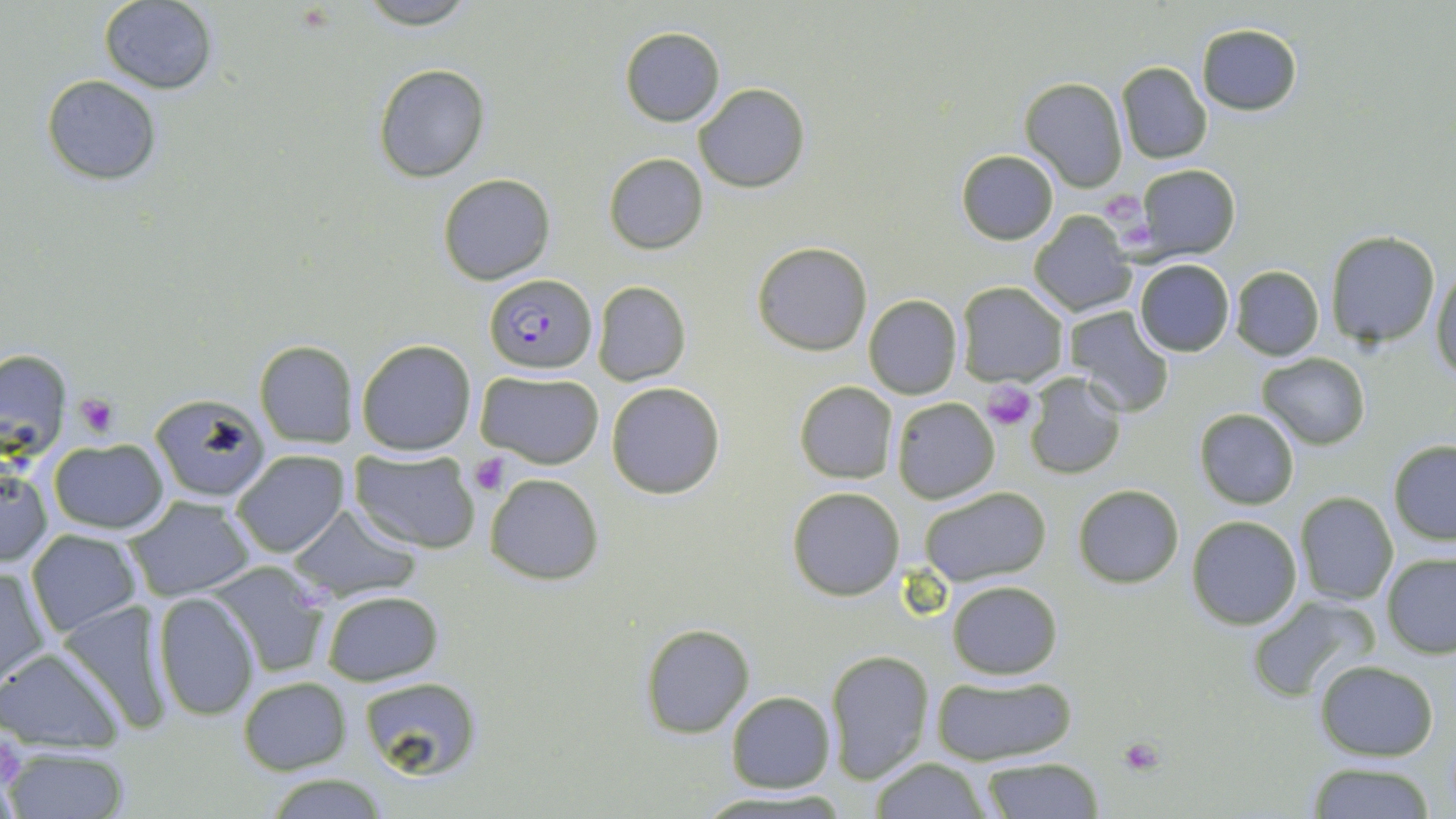
Approximate bounding boxes as [x1, y1, x2, y2] in pixels. Plasmodium falciparum-infected red blood cell locations: [484, 273, 595, 373]. Uninfected red blood cell locations: [353, 0, 482, 28], [98, 1, 219, 93], [1197, 22, 1303, 116], [619, 27, 726, 127], [1116, 61, 1210, 165], [374, 64, 490, 182], [41, 74, 161, 185], [1019, 76, 1128, 191], [694, 83, 810, 193], [955, 149, 1058, 244], [604, 153, 709, 254], [1135, 162, 1239, 259], [438, 173, 555, 284], [1028, 210, 1136, 317], [1325, 231, 1439, 347], [752, 241, 873, 355], [1133, 259, 1234, 357], [1430, 265, 1456, 382], [1230, 266, 1324, 359], [591, 281, 691, 386], [956, 281, 1068, 387], [863, 295, 962, 400], [1061, 306, 1174, 418], [255, 339, 357, 447], [356, 339, 475, 455], [0, 349, 72, 462], [1257, 353, 1369, 450], [474, 369, 606, 468], [1025, 374, 1125, 480], [795, 381, 897, 484], [605, 382, 725, 498], [147, 390, 273, 504], [891, 396, 1001, 504], [1194, 409, 1300, 510], [46, 439, 170, 534], [1388, 439, 1456, 545], [230, 448, 350, 559], [350, 449, 480, 553], [0, 462, 51, 568], [484, 473, 604, 586], [1073, 483, 1185, 587], [787, 486, 904, 600], [918, 486, 1051, 587], [1293, 492, 1399, 606], [125, 497, 257, 602], [288, 504, 424, 601], [1187, 516, 1302, 628], [27, 530, 142, 636], [1383, 552, 1456, 657], [205, 560, 337, 679], [1, 563, 51, 687], [947, 579, 1062, 678], [319, 590, 445, 687], [152, 591, 261, 721], [1246, 595, 1379, 701], [56, 597, 175, 735], [641, 622, 755, 738], [0, 647, 124, 751], [825, 648, 935, 783], [1313, 660, 1439, 760], [357, 672, 485, 783], [932, 675, 1075, 765], [237, 676, 352, 774], [726, 691, 835, 793], [4, 745, 134, 819], [867, 757, 993, 819], [981, 758, 1104, 817], [1306, 761, 1440, 818], [258, 774, 397, 818], [695, 789, 851, 816]. Platelet locations: [1103, 192, 1144, 223], [1117, 222, 1153, 247], [984, 382, 1037, 430], [74, 395, 119, 438], [469, 455, 510, 494], [1118, 736, 1165, 775]. Slide-level diagnosis: Plasmodium falciparum. Image is 1456×819 pixels. Single field of view. Thin blood film. Captured at 1000x magnification. Optical microscopy. May-Grünwald-Giemsa stain.